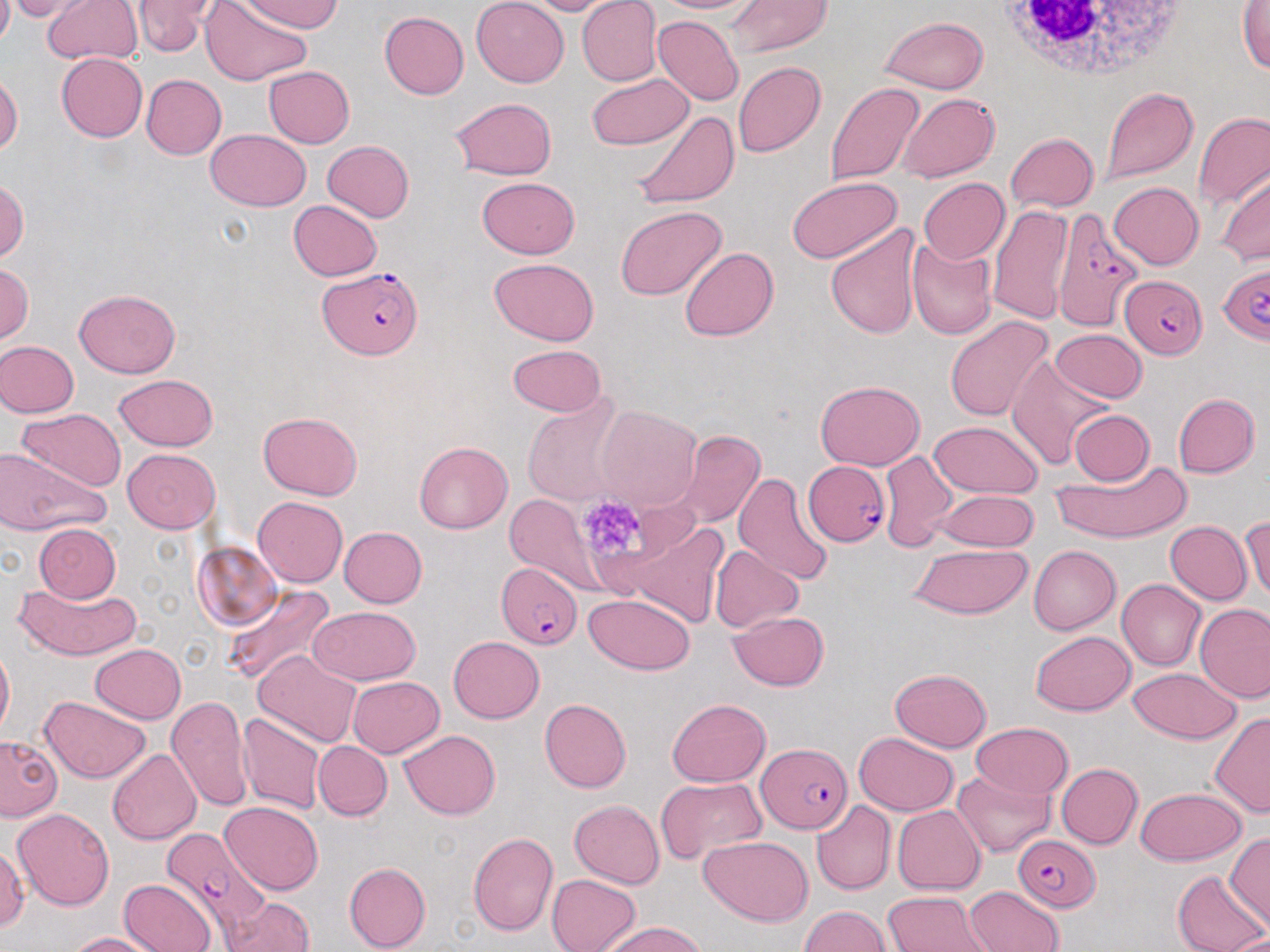

slide-level diagnosis = Plasmodium falciparum
stain = May-Grünwald-Giemsa
modality = optical microscopy
field of view = one of a larger specimen
magnification = 1000x
platelet locations = approximate bounding boxes as (x1,y1)-(x2,y2) corner pairs in pixels: (574,493)-(651,568)
Plasmodium falciparum-infected red blood cell locations = approximate bounding boxes as (x1,y1)-(x2,y2) corner pairs in pixels: (1049,209)-(1142,332), (1217,262)-(1270,344), (319,266)-(421,358), (1120,272)-(1206,358), (804,457)-(889,545), (496,563)-(583,649), (758,743)-(852,833), (163,826)-(272,937), (1012,835)-(1101,912)
preparation = thin blood film
uninfected red blood cell locations = approximate bounding boxes as (x1,y1)-(x2,y2) corner pairs in pixels: (0,0)-(14,51), (3,0)-(95,23), (42,0)-(142,64), (125,0)-(219,56), (200,0)-(314,88), (241,0)-(344,34), (471,0)-(569,87), (518,0)-(620,15), (576,0)-(662,87), (651,0)-(763,15), (725,0)-(833,58), (1238,2)-(1270,76), (379,12)-(469,99), (880,16)-(987,94), (653,17)-(743,105), (56,52)-(147,142), (733,61)-(826,158), (263,66)-(354,147), (1,71)-(22,157), (586,73)-(693,150), (141,74)-(227,160), (824,82)-(926,186), (1101,85)-(1199,186), (896,93)-(999,184), (449,97)-(558,180), (629,109)-(739,210), (1195,114)-(1270,207), (205,129)-(311,211), (1006,132)-(1099,213), (322,141)-(415,222), (1217,171)-(1269,268), (0,176)-(28,264), (786,176)-(903,263), (476,177)-(581,258), (918,178)-(1009,264), (1109,181)-(1203,269), (288,201)-(383,281), (986,202)-(1074,325), (614,206)-(726,301), (825,223)-(925,339), (907,237)-(997,340), (679,246)-(778,342), (489,258)-(600,346), (0,261)-(33,348), (74,288)-(181,377), (944,314)-(1053,422), (1050,329)-(1147,404), (0,341)-(79,417), (508,343)-(608,416), (1007,353)-(1110,472), (113,373)-(219,451), (815,379)-(925,470), (521,391)-(628,508), (1173,393)-(1261,478), (594,405)-(701,512), (17,407)-(126,492), (1069,410)-(1155,486), (258,411)-(363,500), (928,421)-(1043,498), (676,430)-(766,528), (414,441)-(513,533), (3,446)-(109,534), (123,448)-(220,533), (880,449)-(959,552), (1048,455)-(1192,545), (734,472)-(837,587), (934,491)-(1040,551), (506,493)-(598,588), (253,496)-(347,588), (1241,515)-(1270,602), (618,519)-(728,629), (1166,521)-(1253,604), (33,524)-(121,603), (339,527)-(427,607), (193,542)-(282,631), (910,544)-(1034,620), (1029,545)-(1121,634), (710,546)-(804,633), (1117,578)-(1207,671), (15,580)-(141,661), (222,585)-(336,689), (584,592)-(695,674), (1195,604)-(1270,704), (309,606)-(421,685), (728,611)-(829,691), (1030,629)-(1136,716), (448,636)-(543,723), (0,644)-(14,739), (90,644)-(186,723), (253,651)-(363,747), (1128,667)-(1240,744), (889,668)-(994,752), (347,676)-(444,758), (166,695)-(254,812), (39,696)-(152,784), (539,698)-(632,793), (667,698)-(770,787), (1209,711)-(1270,818), (237,713)-(325,814), (971,722)-(1074,799), (399,730)-(500,819), (853,732)-(960,815), (0,735)-(62,821), (314,742)-(392,820), (107,749)-(201,846), (1056,763)-(1143,849), (952,770)-(1057,858), (655,777)-(765,864), (1136,786)-(1247,865), (568,799)-(664,890), (811,801)-(895,895), (220,802)-(325,895), (893,805)-(986,894), (12,808)-(114,910), (468,832)-(559,936), (1226,832)-(1270,931), (699,836)-(813,926), (1,846)-(29,935), (343,861)-(430,952), (1172,870)-(1266,952), (546,874)-(641,952), (119,879)-(216,952), (965,885)-(1065,951), (884,890)-(994,952), (222,897)-(314,952), (798,905)-(891,952), (600,921)-(707,952), (68,932)-(163,952)
white blood cell locations = approximate bounding boxes as (x1,y1)-(x2,y2) corner pairs in pixels: (986,1)-(1198,81)
image size = 1270×952 pixels